Assess this cell for malaria.
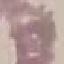
Uninfected.

Summary:
  - Capture: smartphone through the microscope eyepiece
  - Stain: Giemsa
  - Preparation: thin blood film
  - Image type: cell patch, automatically extracted from a larger field of view and resized to 64 × 64 pixels